Describe the morphology of the erythrocytes.
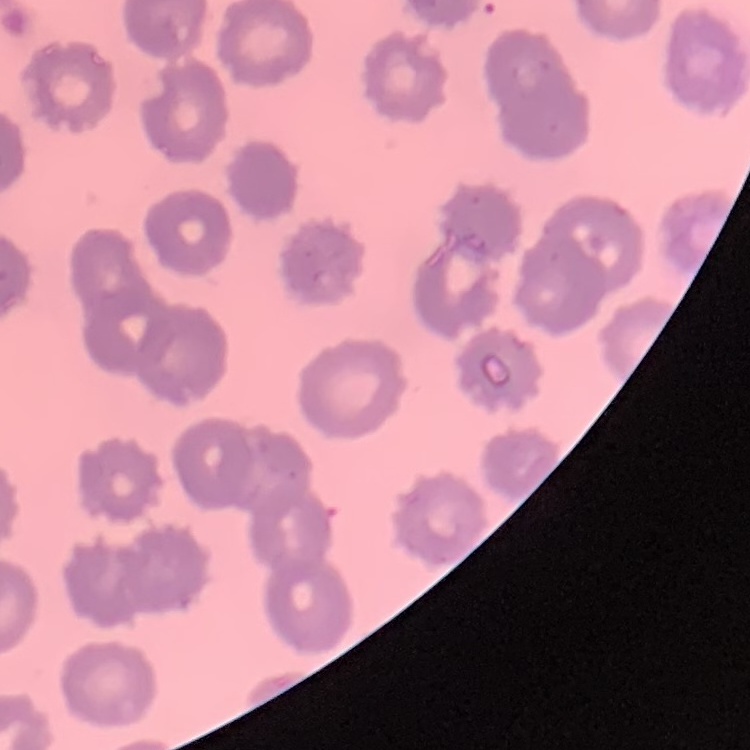
They show no rouleaux formation.

{
  "stain": "Field's or Giemsa",
  "image_type": "square crop of a larger photomicrograph",
  "preparation": "thin peripheral smear"
}